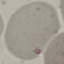 Malaria status: parasitized. Acquired by smartphone through the microscope eyepiece. Thin blood smear. Automatically extracted cell patch, resized to 64 × 64 pixels. Giemsa stain.